Outline each Plasmodium falciparum-infected red blood cell.
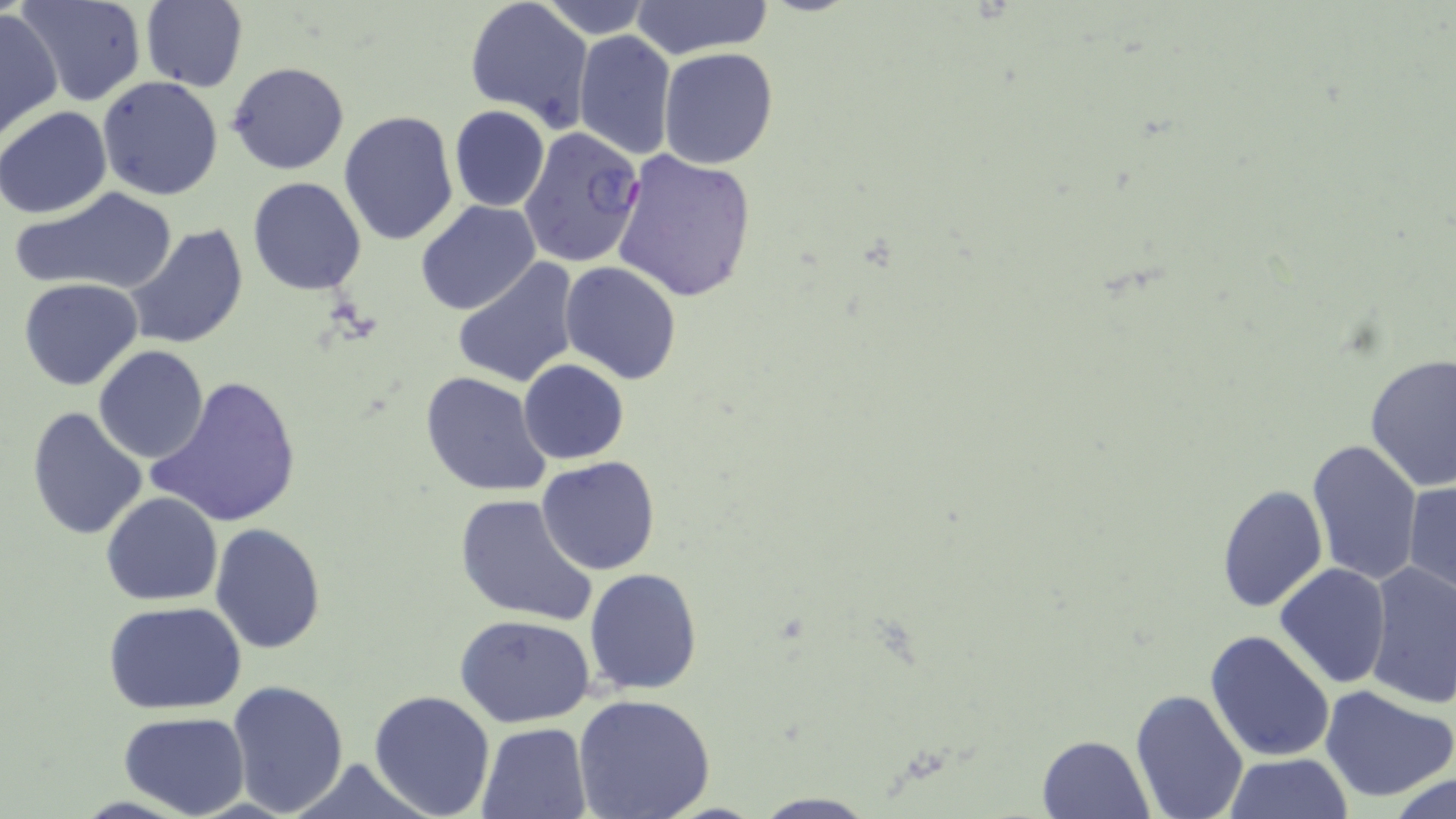
Approximate bounding boxes as (x1, y1, x2, y2) in pixels.
Plasmodium falciparum-infected red blood cells: (517, 126, 647, 270).

slide_level_diagnosis: Plasmodium falciparum
modality: optical microscopy
uninfected_red_blood_cell_locations: 'approximate bounding boxes as (x1, y1, x2, y2) in pixels: (19, 0, 146, 107), (633, 0, 770, 60), (140, 1, 248, 90), (539, 1, 653, 40), (464, 2, 592, 129), (0, 6, 63, 140), (572, 30, 675, 161), (658, 47, 778, 168), (226, 62, 350, 175), (97, 77, 225, 201), (1, 106, 114, 219), (448, 106, 550, 213), (338, 109, 459, 249), (610, 149, 757, 303), (248, 177, 366, 294), (11, 187, 179, 296), (416, 201, 541, 316), (122, 222, 249, 351), (452, 258, 583, 389), (560, 261, 681, 385), (19, 277, 142, 390), (93, 346, 209, 463), (1364, 354, 1456, 490), (519, 359, 629, 464), (419, 371, 552, 496), (147, 374, 302, 528), (26, 406, 149, 542), (1305, 438, 1424, 586), (537, 456, 660, 575), (1404, 480, 1455, 597), (1215, 481, 1326, 615), (101, 491, 222, 605), (454, 491, 598, 626), (209, 522, 327, 653), (1274, 563, 1390, 688), (1363, 563, 1456, 709), (585, 568, 701, 695), (104, 602, 246, 715), (456, 614, 596, 728), (1204, 629, 1335, 763), (224, 678, 349, 817), (1321, 685, 1456, 802), (1130, 687, 1250, 819), (368, 688, 496, 817), (572, 694, 716, 818), (120, 712, 250, 819), (477, 722, 592, 818), (1035, 733, 1154, 819), (1224, 753, 1350, 819), (283, 758, 432, 818), (1386, 773, 1456, 819), (748, 792, 880, 817)'
stain: May-Grünwald-Giemsa
image_size: 1456×819 pixels
field_of_view: one of a larger specimen
magnification: 1000x
preparation: thin blood film